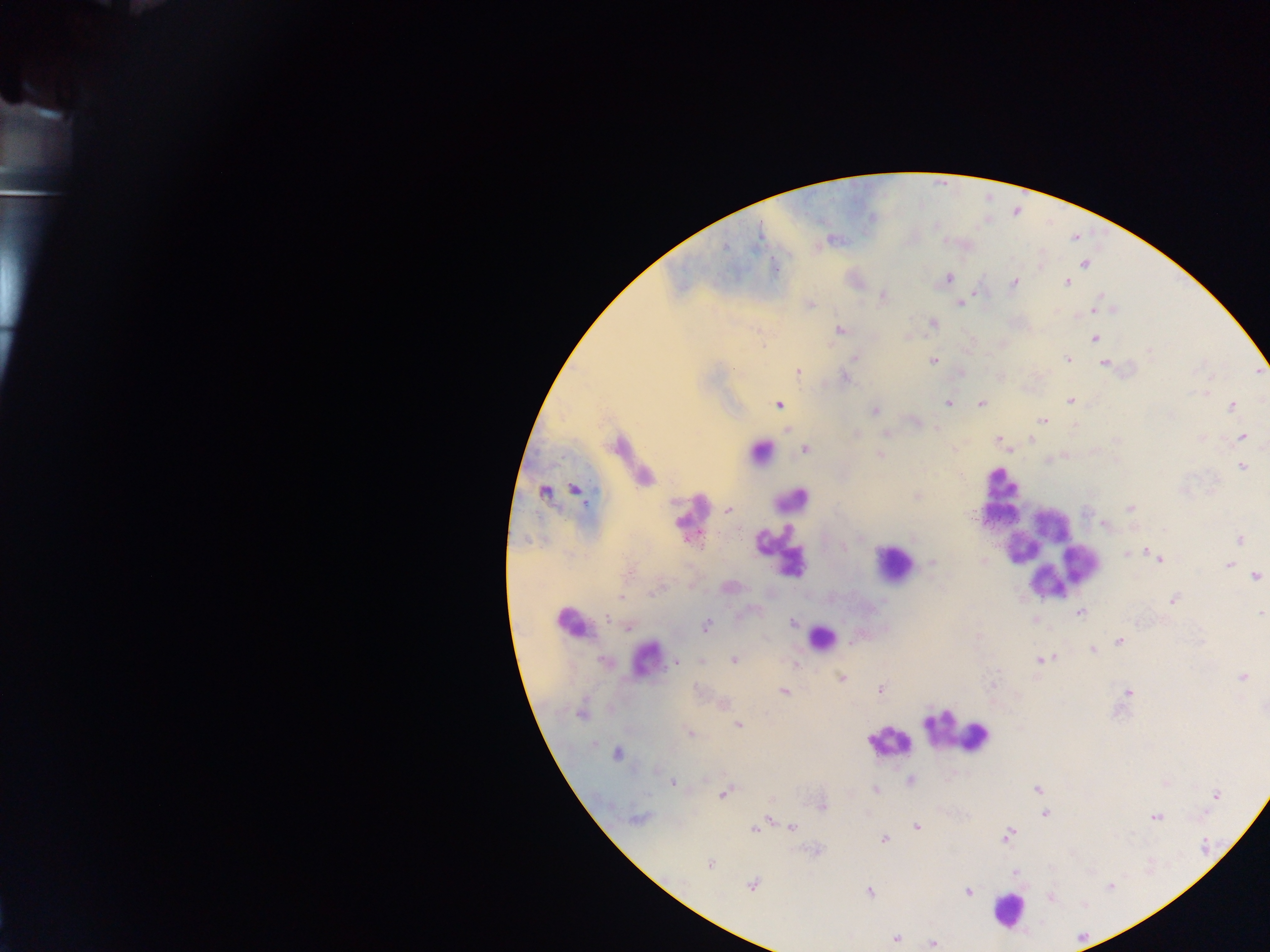
Approximate centers as {x, y} in pixels.
Summary:
  - Plasmodium parasite locations: {1084, 263}, {947, 278}, {1066, 281}, {1013, 283}, {882, 295}, {960, 302}, {809, 304}, {1094, 310}, {932, 323}, {839, 330}, {908, 337}, {1094, 338}, {855, 357}, {1066, 359}, {933, 360}, {1104, 363}, {797, 371}, {844, 377}, {1206, 393}, {1070, 400}, {948, 403}, {981, 403}, {779, 405}, {1231, 405}, {874, 411}, {1042, 421}, {916, 422}, {786, 432}, {886, 433}, {1242, 437}, {1201, 438}, {997, 439}, {1030, 440}, {1010, 450}, {880, 454}, {1242, 466}, {575, 489}, {543, 492}, {916, 497}, {1130, 508}, {728, 510}, {1104, 524}, {860, 536}, {1239, 540}, {1150, 552}, {1128, 553}, {1159, 559}, {933, 562}, {981, 562}, {1227, 565}, {1255, 576}, {621, 598}, {1173, 599}, {1079, 612}, {1259, 613}, {1035, 620}, {793, 622}, {629, 626}, {706, 626}, {1119, 640}, {1092, 649}, {1042, 659}, {733, 660}, {675, 661}, {702, 661}, {841, 677}, {1242, 677}, {993, 684}, {880, 690}, {783, 692}, {1128, 692}, {722, 704}, {581, 711}, {738, 724}, {689, 732}, {616, 754}, {910, 781}, {672, 783}, {1036, 788}, {875, 789}, {725, 792}, {1215, 794}, {821, 805}, {1044, 813}, {1155, 816}, {770, 817}, {637, 818}, {916, 827}, {755, 828}, {791, 828}, {1007, 835}, {883, 839}, {709, 864}, {1014, 872}, {752, 884}, {869, 891}, {967, 891}, {1051, 898}, {895, 938}, {932, 943}
  - Leukocyte locations: {760, 451}, {1003, 486}, {1001, 498}, {789, 499}, {691, 517}, {1031, 530}, {780, 551}, {1050, 556}, {893, 563}, {572, 624}, {820, 638}, {646, 660}, {958, 732}, {976, 739}, {889, 741}, {1008, 910}
  - Country: Ghana
  - Capture: mobile-phone photograph through a microscope
  - Preparation: thick blood smear
  - Field of view: single
  - Image size: 1270×952 pixels